Point out each malaria parasite.
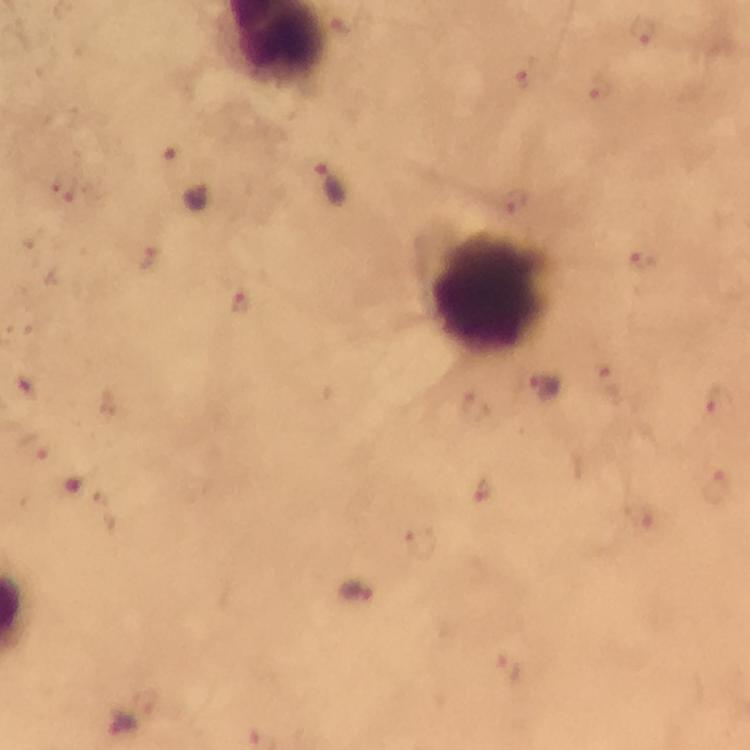

Approximate centers as [x, y] in pixels.
Malaria parasites: [644, 29], [523, 80], [596, 89], [330, 187], [63, 192], [515, 201], [147, 259], [640, 260], [238, 300], [608, 382], [544, 387], [717, 401], [474, 406], [37, 447], [716, 487], [484, 490], [642, 515], [421, 543], [508, 668], [145, 702].

Leukocyte locations: [491, 293]. Photographed through the microscope with a smartphone camera. Cropped region of a single field of view. From a diagnostic examination for malaria. Thick blood film. Immersion oil applied. Image is 750×750 pixels. Giemsa stain. 100x magnification.